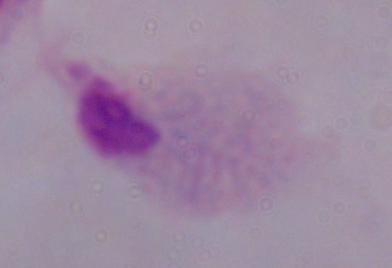

modality: photomicrograph
identification: trichomonad
magnification: 1000x